Identify the cell.
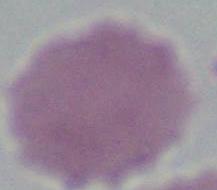

An erythrocyte.

modality = photomicrograph
magnification = 1000x